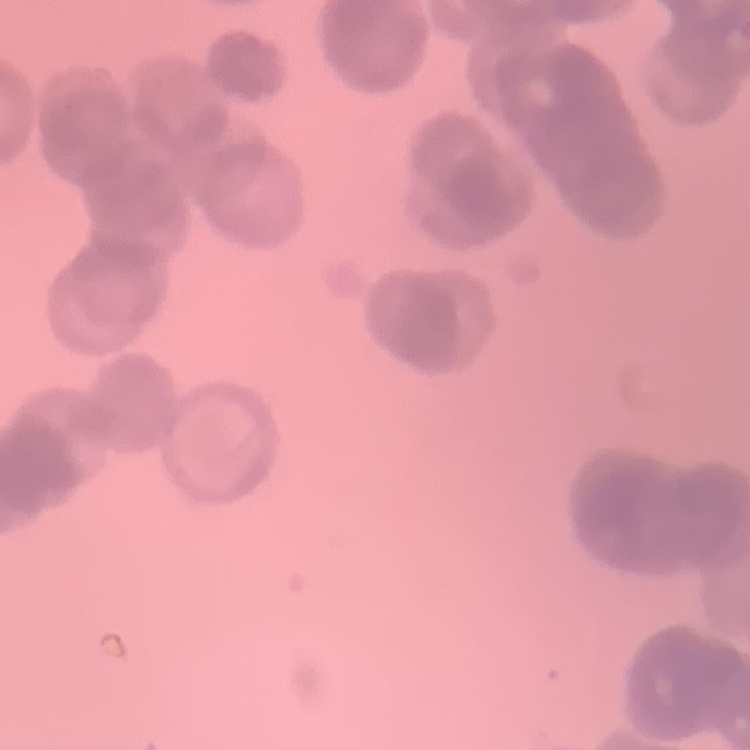
Summary:
  - Erythrocyte morphology: rouleaux formation
  - Stain: Field's or Giemsa
  - Preparation: thin blood smear
  - Image type: square crop of a larger photomicrograph